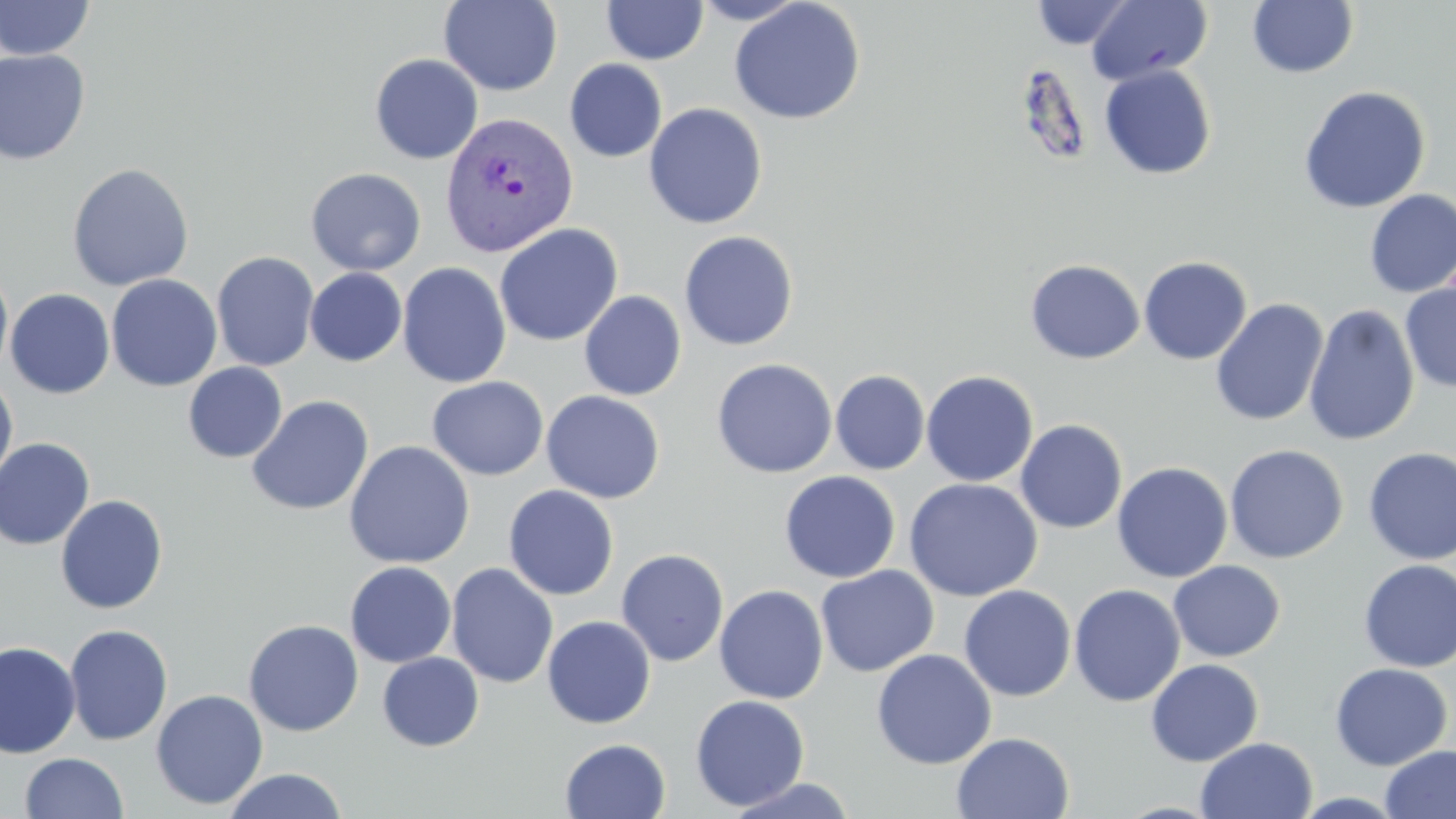
Summary:
  - Coordinate format: approximate bounding boxes as named x1/y1/x2/y2 corners in pixels
  - Plasmodium vivax-infected red blood cell locations: (x1=442, y1=111, x2=578, y2=256)
  - Uninfected red blood cell locations: (x1=0, y1=0, x2=95, y2=61), (x1=691, y1=0, x2=808, y2=25), (x1=1086, y1=0, x2=1212, y2=86), (x1=439, y1=1, x2=563, y2=96), (x1=601, y1=1, x2=708, y2=64), (x1=729, y1=1, x2=866, y2=125), (x1=1031, y1=1, x2=1134, y2=49), (x1=1248, y1=1, x2=1359, y2=79), (x1=0, y1=49, x2=91, y2=165), (x1=370, y1=53, x2=483, y2=165), (x1=564, y1=59, x2=667, y2=162), (x1=1099, y1=64, x2=1217, y2=179), (x1=1298, y1=85, x2=1431, y2=214), (x1=643, y1=103, x2=767, y2=229), (x1=67, y1=162, x2=194, y2=290), (x1=306, y1=167, x2=426, y2=276), (x1=1364, y1=190, x2=1456, y2=298), (x1=494, y1=223, x2=624, y2=346), (x1=679, y1=231, x2=799, y2=351), (x1=211, y1=251, x2=319, y2=372), (x1=1138, y1=256, x2=1252, y2=365), (x1=1025, y1=259, x2=1145, y2=364), (x1=397, y1=262, x2=511, y2=388), (x1=0, y1=264, x2=13, y2=383), (x1=305, y1=267, x2=407, y2=366), (x1=106, y1=274, x2=222, y2=392), (x1=1400, y1=281, x2=1456, y2=393), (x1=4, y1=288, x2=115, y2=399), (x1=579, y1=291, x2=687, y2=400), (x1=1210, y1=298, x2=1329, y2=427), (x1=1304, y1=304, x2=1420, y2=447), (x1=711, y1=358, x2=837, y2=478), (x1=183, y1=362, x2=287, y2=463), (x1=830, y1=369, x2=930, y2=475), (x1=921, y1=370, x2=1038, y2=487), (x1=0, y1=372, x2=18, y2=492), (x1=427, y1=376, x2=549, y2=481), (x1=541, y1=390, x2=665, y2=503), (x1=247, y1=395, x2=374, y2=516), (x1=1015, y1=419, x2=1128, y2=534), (x1=0, y1=438, x2=95, y2=551), (x1=344, y1=440, x2=475, y2=569), (x1=1224, y1=444, x2=1349, y2=563), (x1=1362, y1=447, x2=1456, y2=564), (x1=1112, y1=461, x2=1233, y2=582), (x1=779, y1=470, x2=901, y2=583), (x1=904, y1=477, x2=1042, y2=602), (x1=503, y1=485, x2=620, y2=600), (x1=55, y1=494, x2=168, y2=614), (x1=616, y1=548, x2=729, y2=667), (x1=1358, y1=559, x2=1456, y2=671), (x1=1168, y1=560, x2=1285, y2=662), (x1=345, y1=561, x2=456, y2=668), (x1=446, y1=563, x2=558, y2=688), (x1=816, y1=565, x2=939, y2=677), (x1=714, y1=584, x2=829, y2=704), (x1=958, y1=584, x2=1076, y2=701), (x1=1069, y1=584, x2=1185, y2=706), (x1=541, y1=615, x2=656, y2=729), (x1=243, y1=619, x2=364, y2=736), (x1=63, y1=624, x2=173, y2=745), (x1=0, y1=641, x2=81, y2=759), (x1=871, y1=649, x2=996, y2=770), (x1=378, y1=652, x2=484, y2=751), (x1=1146, y1=658, x2=1264, y2=767), (x1=1329, y1=662, x2=1453, y2=770), (x1=151, y1=688, x2=269, y2=810), (x1=690, y1=694, x2=810, y2=811), (x1=952, y1=732, x2=1074, y2=818), (x1=1196, y1=736, x2=1318, y2=819), (x1=560, y1=738, x2=671, y2=819), (x1=1380, y1=745, x2=1456, y2=819), (x1=20, y1=752, x2=128, y2=818), (x1=222, y1=768, x2=349, y2=819), (x1=725, y1=777, x2=858, y2=818)
  - Slide-level diagnosis: Plasmodium vivax
  - Stain: May-Grünwald-Giemsa
  - Magnification: 1000x
  - Field of view: single
  - Preparation: thin blood film
  - Modality: optical microscopy
  - Image size: 1456×819 pixels